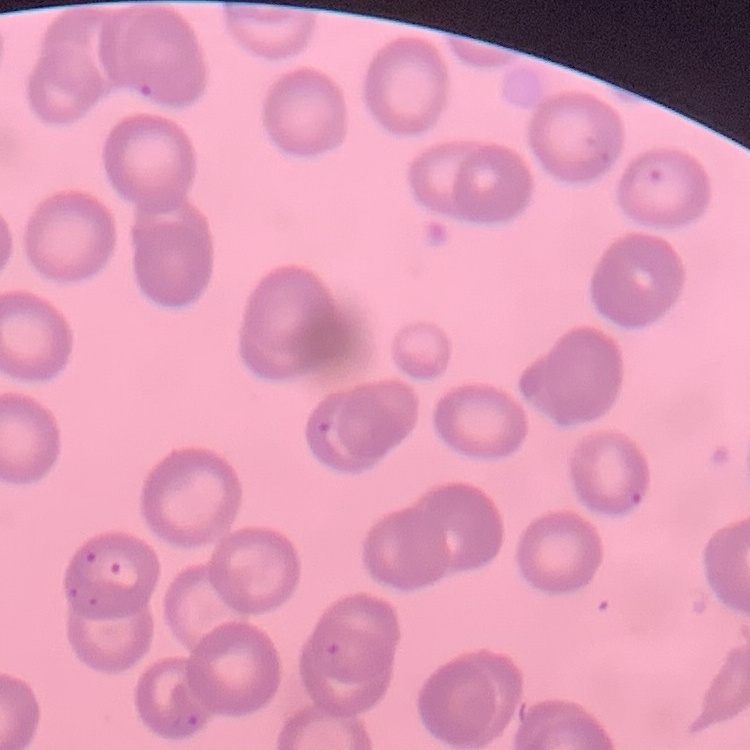 The erythrocytes exhibit no rouleaux formation. Thin peripheral smear. Square crop of a larger photomicrograph. Field's or Giemsa stain.